Comment on the morphology of the red blood cells.
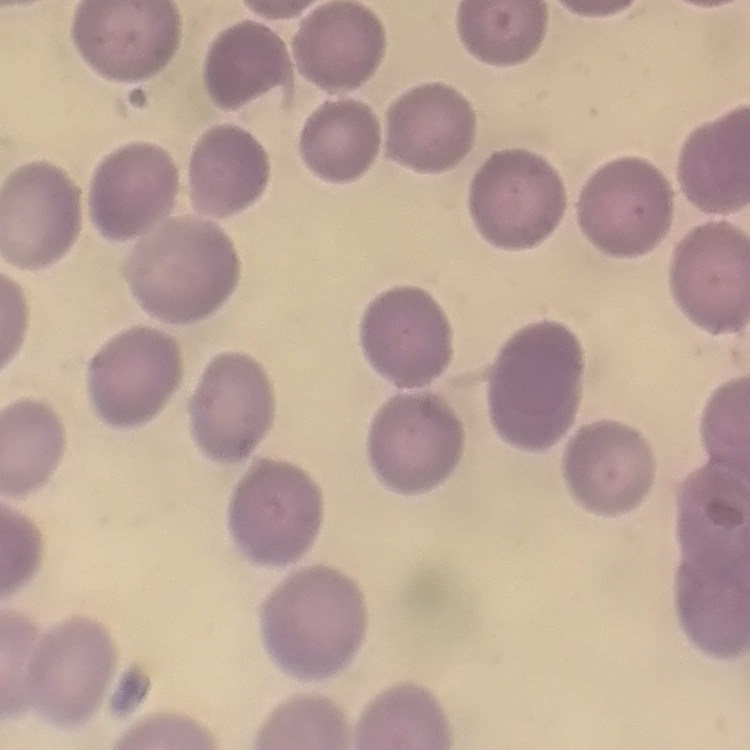

They show no rouleaux formation.

{
  "stain": "Field's or Giemsa",
  "preparation": "thin blood smear",
  "image_type": "one tile cut from a larger photomicrograph"
}